Give a bounding box for every malaria parasite, every leukocyte, and every artifact (stain precipitate or debris).
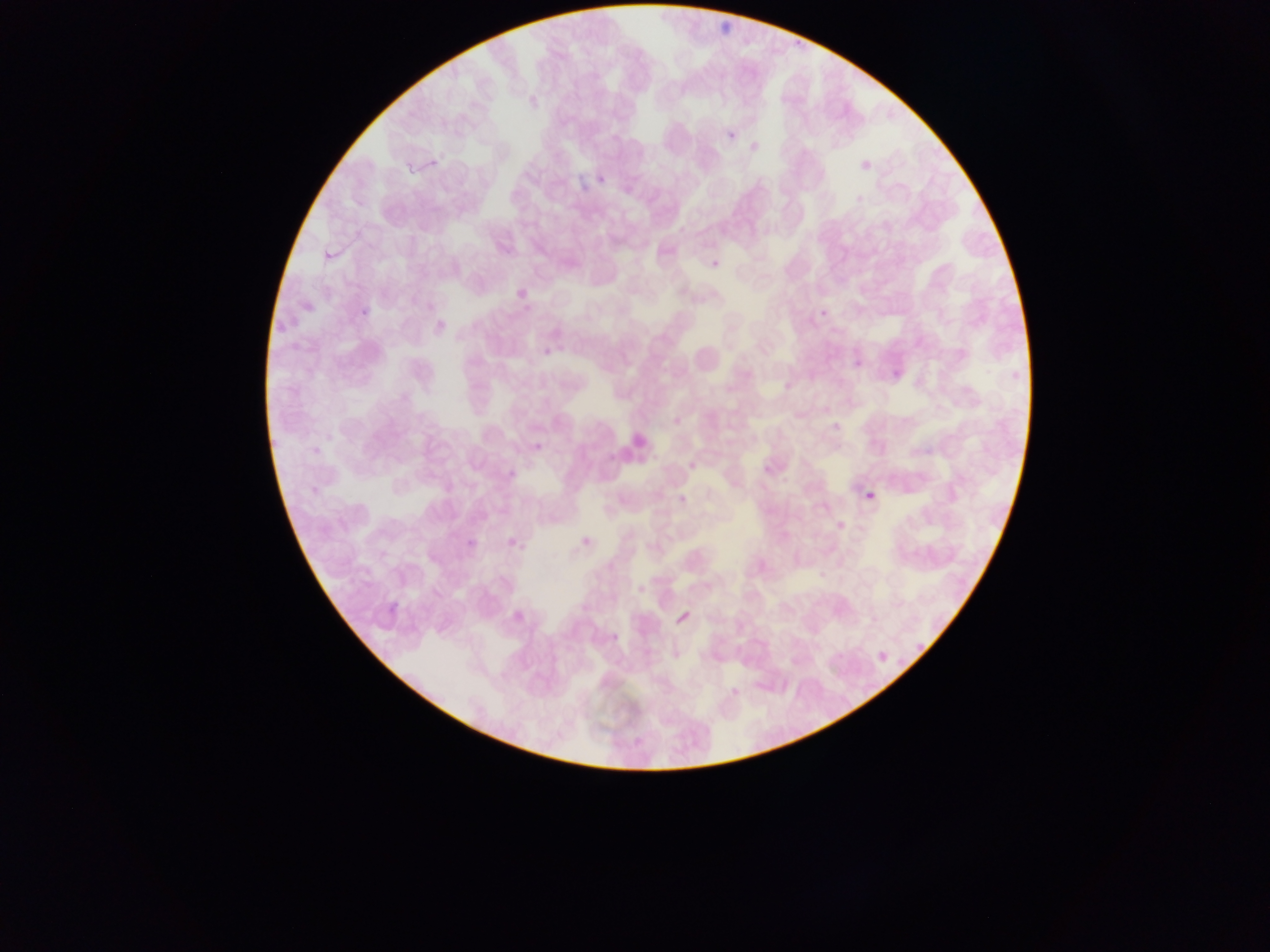

Approximate bounding boxes as {left, top, right, bottom} in pixels.
No malaria parasites observed.
Leukocytes: {612, 431, 653, 465}.

Summary:
  - Capture: mobile-phone photograph through a microscope
  - Image size: 1270×952 pixels
  - Country: Ghana
  - Preparation: thin blood film
  - Field of view: single